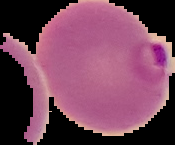

image type = segmented cell region on a black background
image size = 175×145 pixels
malaria status = parasitized
preparation = thin blood smear